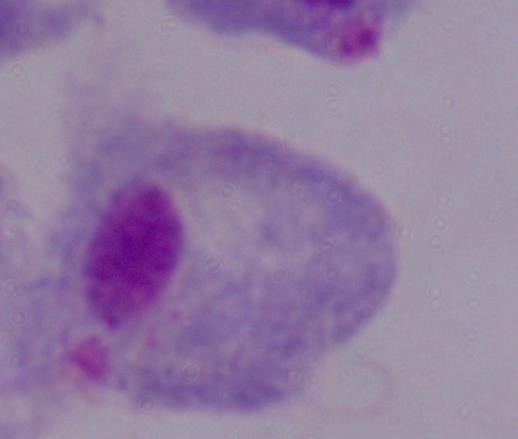

A trichomonad is shown. 1000x magnification. Photomicrograph.